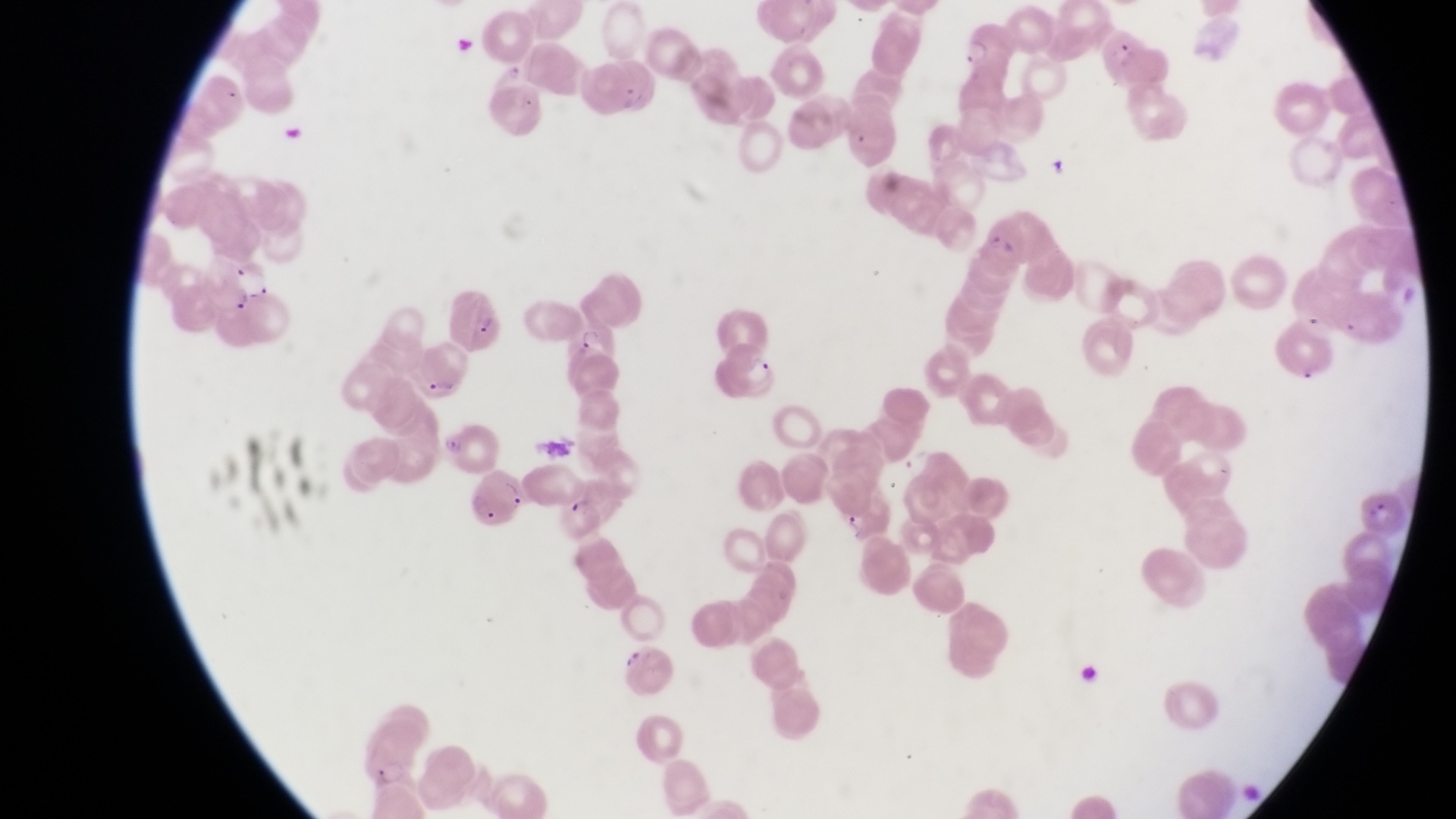
magnification = 1000x
country = Uganda
preparation = thin blood smear
field of view = single
artifact (platelet-like body, stain precipitate, or debris) locations = approximate bounding boxes as [left, top, right, bottom] in pixels: [452, 33, 481, 56], [284, 116, 305, 145]
image size = 1456×819 pixels
parasitised red blood cell locations = approximate bounding boxes as [left, top, right, bottom] in pixels: [957, 16, 1015, 72], [1100, 24, 1150, 80], [594, 55, 658, 119], [981, 212, 1054, 268], [195, 256, 274, 320], [452, 281, 510, 361], [571, 317, 621, 372], [720, 340, 779, 400], [412, 341, 467, 402], [436, 416, 510, 469], [469, 470, 525, 528], [557, 489, 612, 541], [1364, 491, 1407, 537], [618, 639, 681, 699], [351, 727, 418, 788]
capture = smartphone photograph through the eyepiece of an Olympus CX-23 microscope